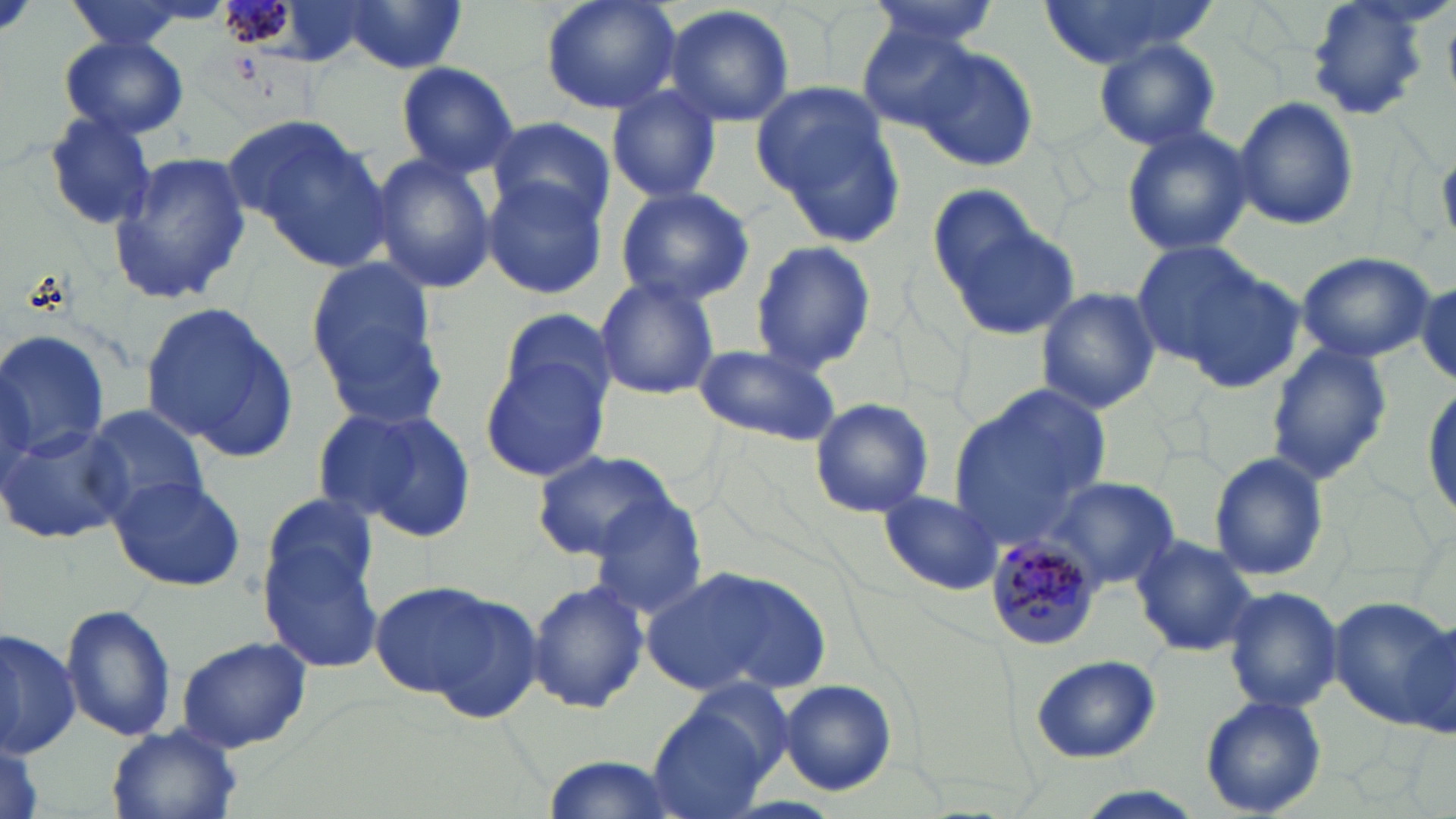
Plasmodium malariae-infected red blood cell locations = approximate bounding boxes as (x1,y1)-(x2,y2) corner pairs in pixels: (985,540)-(1103,653)
slide-level diagnosis = Plasmodium malariae
uninfected red blood cell locations = approximate bounding boxes as (x1,y1)-(x2,y2) corner pairs in pixels: (59,0)-(221,55), (539,0)-(682,116), (863,0)-(999,51), (1037,0)-(1214,71), (1305,0)-(1437,119), (336,1)-(470,74), (663,4)-(796,129), (857,23)-(985,133), (56,34)-(189,140), (1093,39)-(1222,150), (912,43)-(1040,171), (395,62)-(519,176), (754,80)-(905,242), (605,84)-(721,203), (1234,97)-(1359,232), (40,111)-(156,231), (227,111)-(383,252), (487,115)-(615,226), (1121,122)-(1253,259), (107,149)-(252,304), (369,153)-(497,294), (483,175)-(608,300), (613,184)-(757,306), (938,199)-(1080,340), (749,240)-(877,374), (1134,244)-(1299,389), (1294,251)-(1435,364), (304,253)-(442,410), (595,276)-(720,400), (1415,278)-(1453,384), (1035,286)-(1161,414), (139,298)-(299,461), (497,307)-(618,414), (0,328)-(109,462), (693,342)-(842,446), (1267,345)-(1394,482), (480,352)-(613,480), (950,384)-(1112,544), (1422,384)-(1454,522), (809,396)-(935,518), (80,405)-(211,521), (323,406)-(479,543), (1,422)-(128,546), (531,450)-(682,561), (1209,453)-(1328,580), (111,475)-(247,593), (1050,477)-(1179,591), (261,490)-(376,599), (880,490)-(1003,596), (583,500)-(709,621), (259,532)-(387,674), (1131,534)-(1258,658), (643,563)-(828,700), (369,580)-(501,699), (526,580)-(650,713), (1223,586)-(1343,716), (421,592)-(545,727), (1329,595)-(1454,725), (61,607)-(176,741), (1395,617)-(1454,745), (0,624)-(81,759), (174,636)-(312,753), (1028,654)-(1161,765), (675,673)-(797,789), (776,679)-(899,794), (1200,695)-(1329,817), (648,705)-(777,819), (106,723)-(243,819), (0,738)-(45,819), (537,754)-(682,818), (1071,787)-(1207,818)
modality = optical microscopy
magnification = 1000x
image size = 1456×819 pixels
preparation = thin blood film
stain = May-Grünwald-Giemsa
field of view = one of a larger specimen